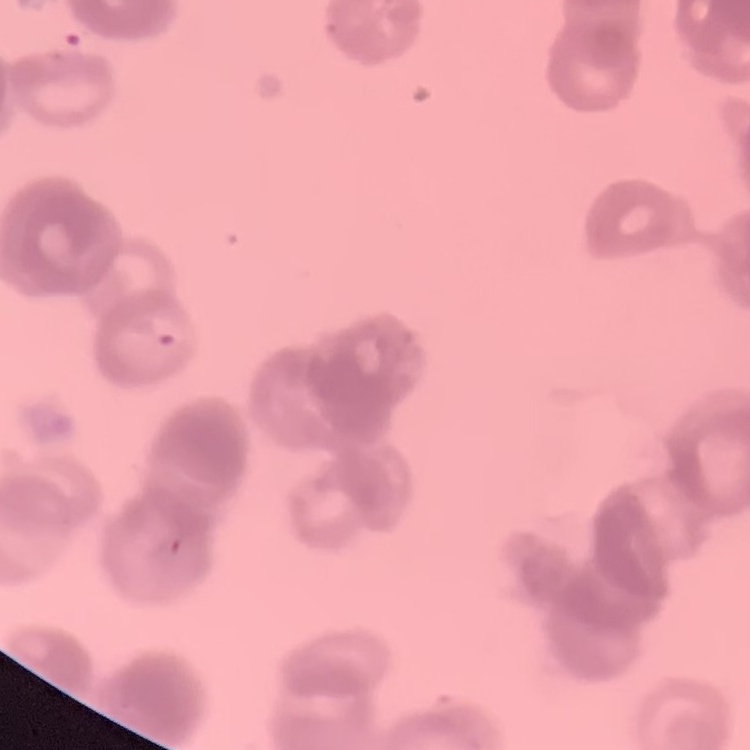 The red blood cells show rouleaux formation. Thin blood film. One tile cut from a larger photomicrograph. Field's or Giemsa stain.